Describe the morphology of the erythrocytes.
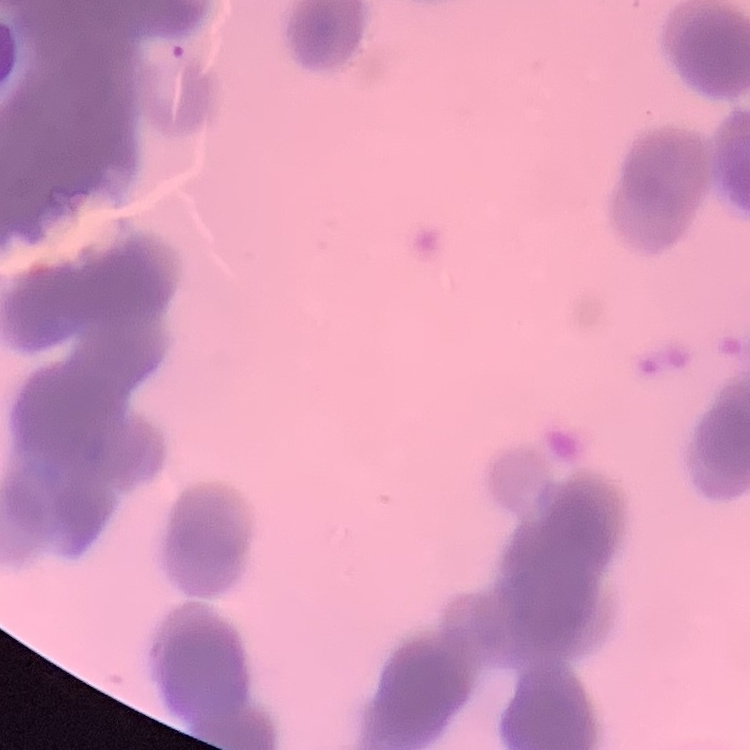
They show rouleaux formation.

Stained with either Field's or Giemsa. One tile cut from a larger photomicrograph. Thin peripheral smear.